Give the location of every parasitized red blood cell.
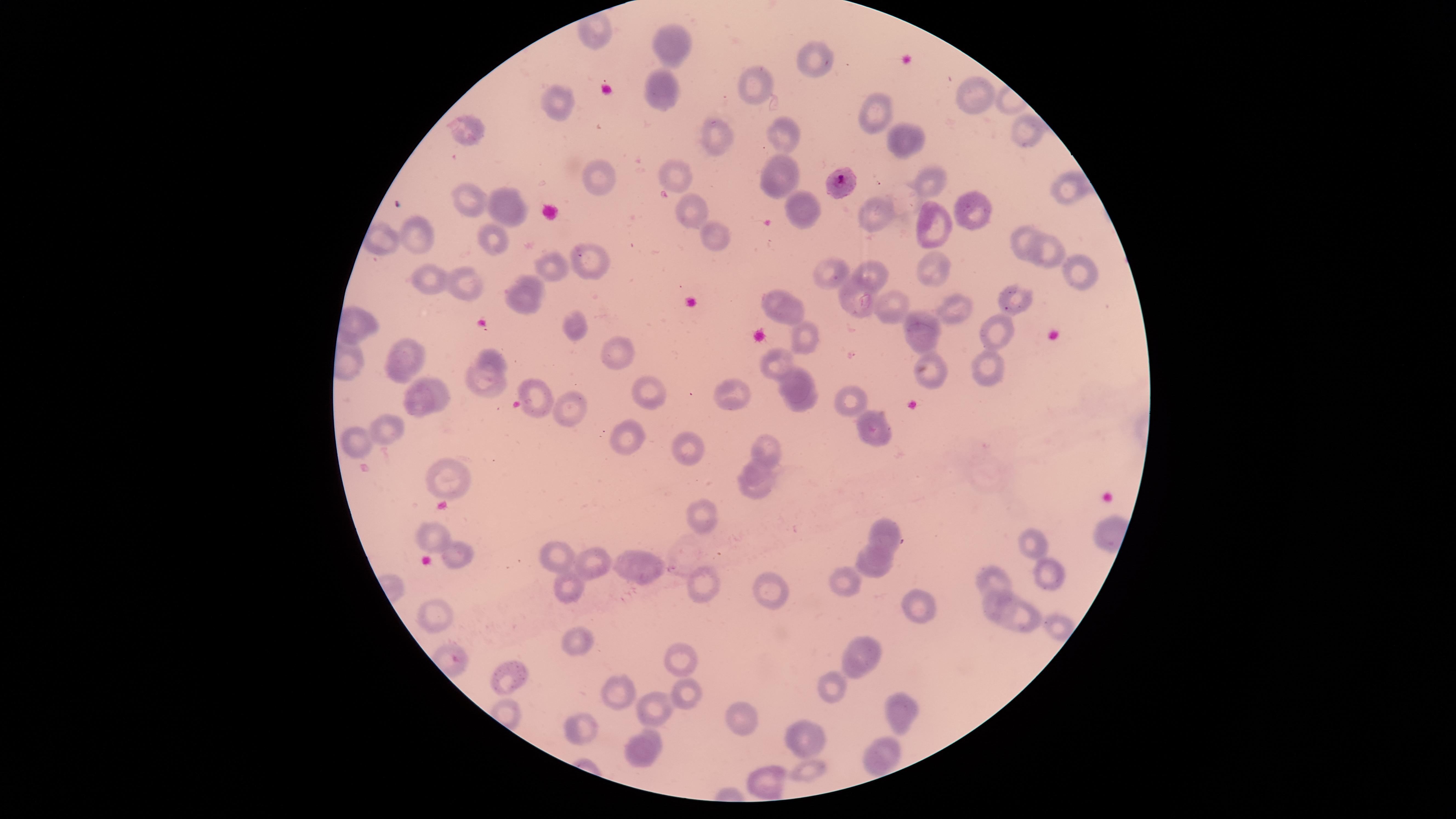
Approximate marker points, in pixels from the top-left corner.
Parasitized red blood cells: (x=837, y=184).

field_of_view: single
image_size: 1456×819 pixels
preparation: thin blood film
uninfected_red_blood_cells: 'approximate marker points, in pixels from the top-left corner: (x=679, y=44), (x=813, y=62), (x=663, y=87), (x=759, y=87), (x=959, y=89), (x=561, y=104), (x=869, y=108), (x=1019, y=125), (x=472, y=127), (x=785, y=129), (x=718, y=137), (x=899, y=139), (x=922, y=172), (x=679, y=176), (x=775, y=176), (x=597, y=178), (x=1064, y=184), (x=470, y=197), (x=505, y=207), (x=805, y=207), (x=687, y=210), (x=973, y=211), (x=879, y=212), (x=942, y=225), (x=426, y=236), (x=491, y=238), (x=1025, y=241), (x=715, y=243), (x=1050, y=256), (x=586, y=260), (x=930, y=264), (x=1076, y=266), (x=832, y=268), (x=561, y=271), (x=875, y=273), (x=531, y=281), (x=432, y=282), (x=470, y=288), (x=1010, y=297), (x=856, y=299), (x=522, y=300), (x=951, y=307), (x=892, y=308), (x=786, y=315), (x=924, y=319), (x=1000, y=325), (x=580, y=334), (x=806, y=336), (x=922, y=340), (x=609, y=349), (x=406, y=360), (x=780, y=361), (x=989, y=361), (x=496, y=363), (x=928, y=373), (x=794, y=383), (x=482, y=384), (x=645, y=389), (x=438, y=394), (x=733, y=394), (x=538, y=395), (x=418, y=398), (x=851, y=402), (x=573, y=403), (x=802, y=404), (x=880, y=429), (x=384, y=431), (x=632, y=437), (x=363, y=438), (x=690, y=448), (x=769, y=452), (x=756, y=467), (x=450, y=472), (x=754, y=490), (x=707, y=514), (x=891, y=533), (x=428, y=536), (x=1027, y=540), (x=881, y=553), (x=562, y=555), (x=456, y=557), (x=594, y=558), (x=623, y=560), (x=639, y=563), (x=1052, y=571), (x=874, y=573), (x=994, y=576), (x=701, y=585), (x=570, y=587), (x=851, y=587), (x=769, y=588), (x=918, y=600), (x=995, y=605), (x=431, y=611), (x=1018, y=615), (x=1056, y=627), (x=583, y=644), (x=871, y=646), (x=684, y=660), (x=852, y=672), (x=510, y=676), (x=831, y=686), (x=614, y=693), (x=685, y=694), (x=900, y=703), (x=657, y=707), (x=745, y=718), (x=586, y=733), (x=804, y=736), (x=652, y=737), (x=886, y=745), (x=639, y=754), (x=871, y=764), (x=806, y=773), (x=766, y=781)'
visible_region: circular
capture: smartphone photograph through the microscope eyepiece
stain: Giemsa
species: Plasmodium falciparum